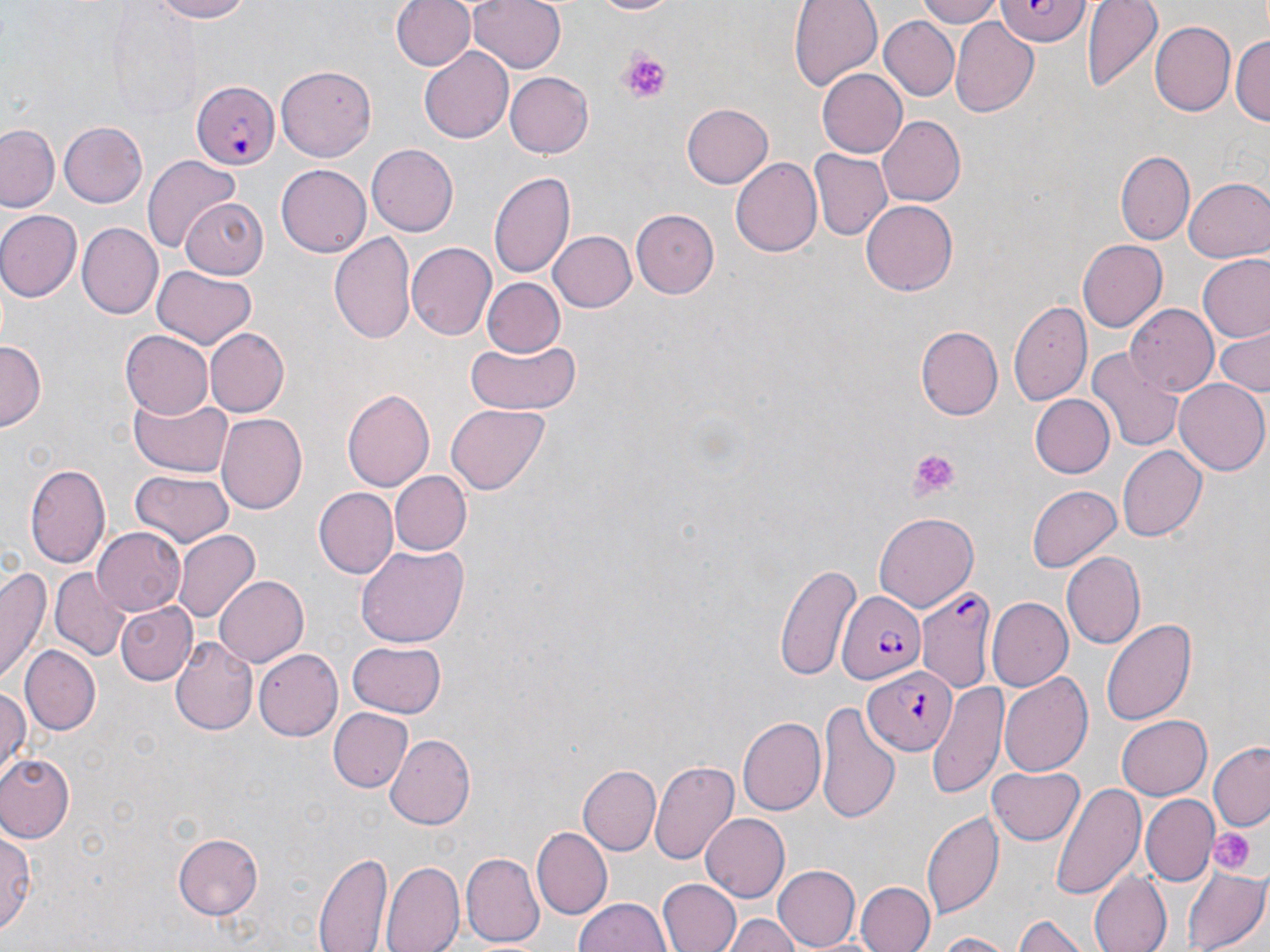

Summary:
  - Coordinate format: approximate bounding boxes as (x1, y1, x2, y2) in pixels
  - Platelet locations: (617, 51, 674, 103), (906, 447, 957, 499), (1211, 828, 1253, 872)
  - Uninfected red blood cell locations: (145, 0, 257, 23), (393, 0, 476, 71), (468, 0, 565, 75), (582, 0, 682, 17), (788, 0, 881, 91), (917, 0, 1007, 27), (1081, 0, 1162, 93), (108, 7, 200, 110), (880, 17, 958, 101), (951, 20, 1039, 117), (1150, 22, 1235, 115), (1179, 26, 1269, 122), (1232, 32, 1270, 128), (419, 44, 514, 139), (277, 63, 376, 158), (817, 69, 907, 158), (504, 71, 593, 158), (682, 103, 773, 189), (877, 115, 967, 207), (59, 122, 148, 206), (1, 124, 61, 211), (367, 142, 459, 238), (807, 149, 891, 241), (1116, 151, 1193, 243), (141, 153, 240, 253), (732, 159, 821, 255), (276, 165, 370, 257), (489, 169, 575, 279), (1185, 177, 1269, 264), (862, 200, 957, 296), (179, 201, 268, 275), (630, 209, 718, 298), (1, 211, 82, 300), (76, 221, 162, 317), (549, 230, 636, 313), (328, 231, 417, 344), (1076, 239, 1165, 331), (406, 241, 497, 340), (1199, 254, 1270, 340), (152, 266, 257, 349), (484, 277, 565, 355), (1010, 297, 1090, 409), (1124, 303, 1220, 394), (204, 326, 289, 418), (915, 326, 1003, 421), (1212, 327, 1270, 398), (120, 331, 212, 419), (463, 338, 582, 415), (0, 342, 44, 428), (1090, 347, 1184, 453), (1173, 378, 1267, 475), (341, 389, 434, 492), (1028, 393, 1115, 478), (131, 394, 233, 473), (447, 404, 549, 494), (215, 414, 306, 515), (1118, 446, 1206, 540), (25, 460, 111, 572), (130, 468, 234, 546), (392, 471, 470, 555), (1025, 484, 1121, 570), (313, 487, 398, 579), (873, 512, 979, 612), (91, 527, 183, 616), (172, 529, 260, 624), (357, 543, 470, 649), (1060, 549, 1146, 648), (775, 562, 861, 679), (2, 563, 53, 686), (50, 566, 133, 660), (214, 574, 309, 665), (988, 597, 1073, 692), (116, 602, 195, 684), (1102, 616, 1198, 726), (171, 635, 257, 736), (347, 641, 446, 716), (19, 645, 99, 735), (253, 650, 341, 742), (999, 675, 1093, 778), (928, 682, 1007, 797), (0, 687, 29, 777), (817, 704, 899, 822), (328, 708, 414, 794), (1117, 714, 1211, 799), (739, 716, 825, 814), (385, 732, 476, 828), (1210, 743, 1270, 831), (0, 755, 75, 842), (649, 760, 739, 865), (578, 764, 659, 854), (989, 764, 1084, 844), (1050, 782, 1143, 900), (1141, 793, 1218, 884), (922, 809, 1004, 921), (701, 814, 790, 902), (0, 827, 37, 938), (534, 827, 610, 915), (174, 833, 263, 918), (314, 850, 390, 951), (460, 851, 544, 948), (382, 861, 463, 952), (772, 864, 859, 950), (1183, 864, 1269, 952), (1089, 872, 1169, 952), (658, 878, 740, 952), (855, 881, 934, 952), (574, 897, 671, 952), (727, 915, 801, 952), (1013, 915, 1089, 952), (930, 931, 1020, 951)
  - Plasmodium falciparum-infected red blood cell locations: (993, 0, 1091, 44), (193, 80, 280, 171), (919, 590, 994, 695), (835, 592, 926, 685), (863, 666, 957, 757)
  - Slide-level diagnosis: Plasmodium falciparum
  - Field of view: single
  - Magnification: 1000x
  - Stain: May-Grünwald-Giemsa
  - Preparation: thin blood smear
  - Modality: optical microscopy
  - Image size: 1270×952 pixels